Locate and identify every blood parasite.
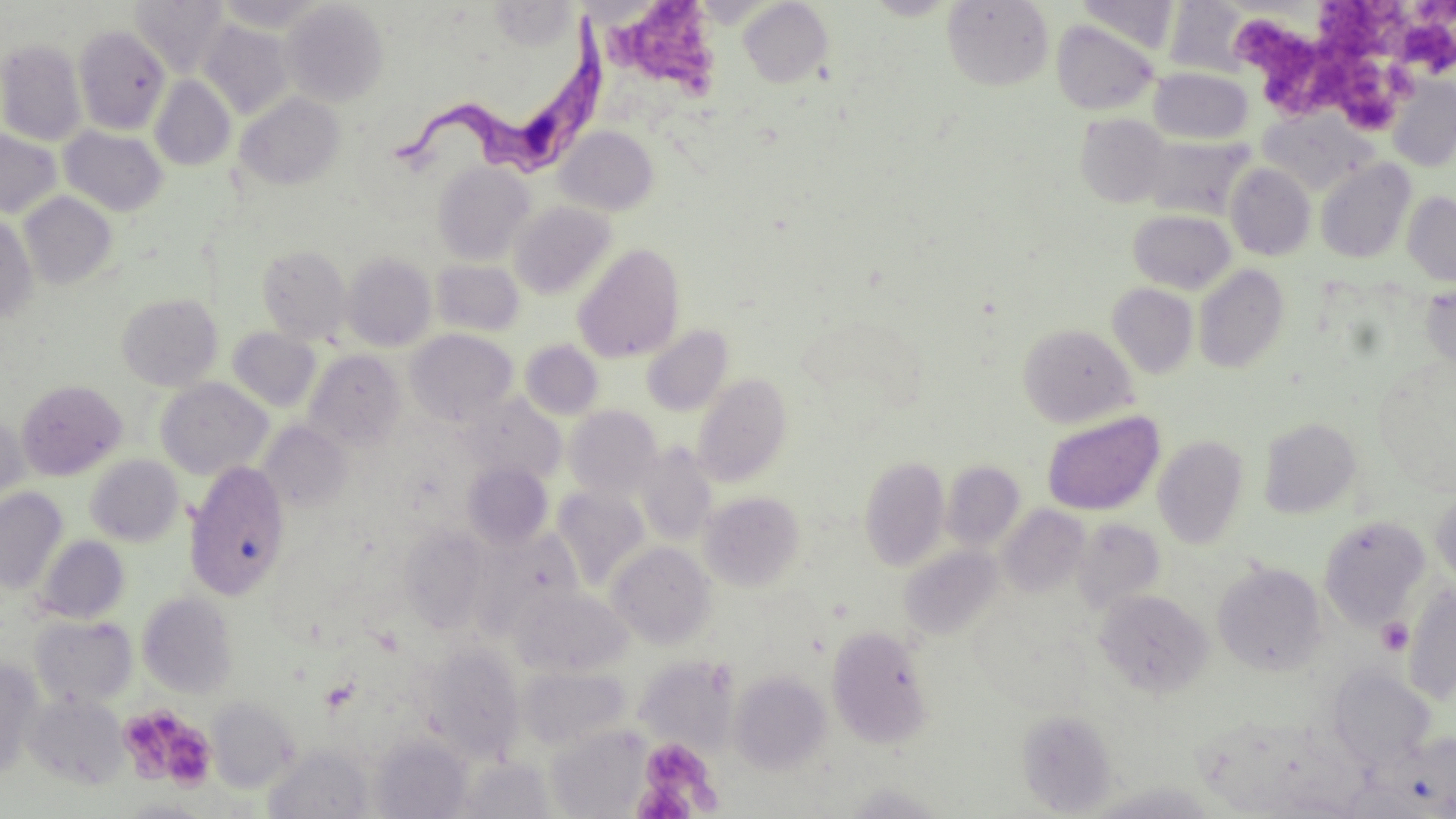
Approximate bounding boxes as named x1/y1/x2/y2 corners in pixels.
Trypanosoma brucei: (x1=393, y1=11, x2=605, y2=191).
No Plasmodium falciparum, Plasmodium ovale, Plasmodium malariae, Plasmodium vivax, or Babesia divergens observed.

Platelet locations: (x1=611, y1=2, x2=719, y2=103), (x1=1397, y1=2, x2=1456, y2=76), (x1=1315, y1=3, x2=1404, y2=58), (x1=1237, y1=19, x2=1315, y2=86), (x1=1275, y1=37, x2=1401, y2=128), (x1=1377, y1=617, x2=1414, y2=656), (x1=119, y1=708, x2=214, y2=791), (x1=637, y1=738, x2=717, y2=810), (x1=632, y1=782, x2=694, y2=818). Uninfected red blood cell locations: (x1=131, y1=0, x2=229, y2=77), (x1=211, y1=0, x2=329, y2=32), (x1=942, y1=0, x2=1054, y2=92), (x1=1074, y1=0, x2=1181, y2=54), (x1=739, y1=1, x2=832, y2=87), (x1=281, y1=2, x2=388, y2=106), (x1=1163, y1=2, x2=1252, y2=77), (x1=1051, y1=19, x2=1160, y2=115), (x1=199, y1=21, x2=294, y2=119), (x1=73, y1=25, x2=170, y2=134), (x1=0, y1=39, x2=87, y2=146), (x1=1149, y1=68, x2=1253, y2=144), (x1=150, y1=75, x2=235, y2=171), (x1=1386, y1=75, x2=1455, y2=172), (x1=235, y1=92, x2=345, y2=191), (x1=1258, y1=110, x2=1375, y2=196), (x1=1076, y1=114, x2=1171, y2=207), (x1=59, y1=125, x2=168, y2=216), (x1=555, y1=126, x2=659, y2=216), (x1=0, y1=129, x2=62, y2=218), (x1=1141, y1=135, x2=1253, y2=219), (x1=1316, y1=158, x2=1416, y2=264), (x1=433, y1=162, x2=535, y2=265), (x1=1225, y1=163, x2=1316, y2=261), (x1=19, y1=191, x2=117, y2=289), (x1=1403, y1=191, x2=1456, y2=287), (x1=509, y1=201, x2=616, y2=300), (x1=1128, y1=209, x2=1236, y2=294), (x1=0, y1=212, x2=38, y2=324), (x1=257, y1=244, x2=351, y2=343), (x1=573, y1=244, x2=685, y2=363), (x1=342, y1=252, x2=436, y2=351), (x1=431, y1=258, x2=524, y2=337), (x1=1194, y1=264, x2=1290, y2=373), (x1=1419, y1=282, x2=1456, y2=374), (x1=1107, y1=283, x2=1198, y2=378), (x1=116, y1=292, x2=222, y2=390), (x1=797, y1=313, x2=927, y2=423), (x1=1018, y1=323, x2=1137, y2=428), (x1=642, y1=325, x2=732, y2=414), (x1=228, y1=327, x2=320, y2=412), (x1=405, y1=328, x2=518, y2=426), (x1=520, y1=339, x2=604, y2=420), (x1=304, y1=350, x2=406, y2=451), (x1=692, y1=373, x2=793, y2=487), (x1=155, y1=378, x2=272, y2=479), (x1=17, y1=379, x2=127, y2=480), (x1=459, y1=394, x2=566, y2=485), (x1=564, y1=405, x2=662, y2=500), (x1=0, y1=412, x2=28, y2=505), (x1=1042, y1=412, x2=1164, y2=515), (x1=1258, y1=417, x2=1361, y2=518), (x1=259, y1=421, x2=351, y2=513), (x1=1153, y1=435, x2=1249, y2=549), (x1=634, y1=442, x2=717, y2=546), (x1=85, y1=455, x2=185, y2=546), (x1=859, y1=455, x2=950, y2=571), (x1=184, y1=460, x2=290, y2=600), (x1=941, y1=461, x2=1025, y2=553), (x1=462, y1=462, x2=553, y2=550), (x1=552, y1=487, x2=650, y2=588), (x1=0, y1=488, x2=68, y2=593), (x1=1430, y1=490, x2=1456, y2=588), (x1=700, y1=491, x2=805, y2=591), (x1=998, y1=505, x2=1090, y2=598), (x1=1319, y1=516, x2=1430, y2=629), (x1=1072, y1=518, x2=1165, y2=613), (x1=398, y1=525, x2=490, y2=631), (x1=471, y1=527, x2=585, y2=638), (x1=35, y1=536, x2=129, y2=624), (x1=607, y1=541, x2=717, y2=649), (x1=899, y1=545, x2=1004, y2=641), (x1=1213, y1=561, x2=1326, y2=676), (x1=1402, y1=584, x2=1456, y2=703), (x1=512, y1=586, x2=631, y2=676), (x1=1094, y1=589, x2=1213, y2=697), (x1=138, y1=592, x2=238, y2=698), (x1=30, y1=615, x2=137, y2=708), (x1=826, y1=624, x2=934, y2=748), (x1=423, y1=642, x2=525, y2=762), (x1=635, y1=656, x2=737, y2=753), (x1=0, y1=660, x2=43, y2=780), (x1=519, y1=666, x2=630, y2=752), (x1=1328, y1=666, x2=1435, y2=769), (x1=730, y1=671, x2=831, y2=773), (x1=25, y1=693, x2=128, y2=789), (x1=206, y1=697, x2=299, y2=793), (x1=1017, y1=708, x2=1117, y2=816), (x1=548, y1=727, x2=649, y2=818), (x1=1389, y1=733, x2=1456, y2=816), (x1=371, y1=735, x2=471, y2=818), (x1=264, y1=744, x2=375, y2=818), (x1=457, y1=757, x2=554, y2=818), (x1=841, y1=782, x2=950, y2=818), (x1=1082, y1=782, x2=1221, y2=819), (x1=119, y1=798, x2=211, y2=817). Slide-level diagnosis: Trypanosoma brucei. Light microscopy. May-Grünwald-Giemsa stain. One field of a larger specimen. Image is 1456×819 pixels. 1000x magnification. Thin blood smear.